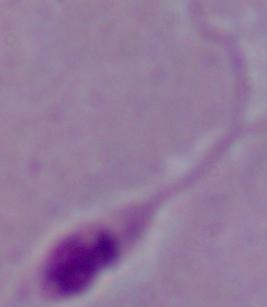 Photomicrograph. 1000x magnification. A Leishmania parasite is shown.